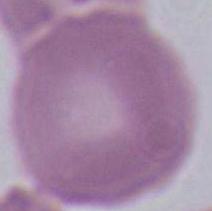 Photomicrograph. 1000x magnification. An erythrocyte is seen.